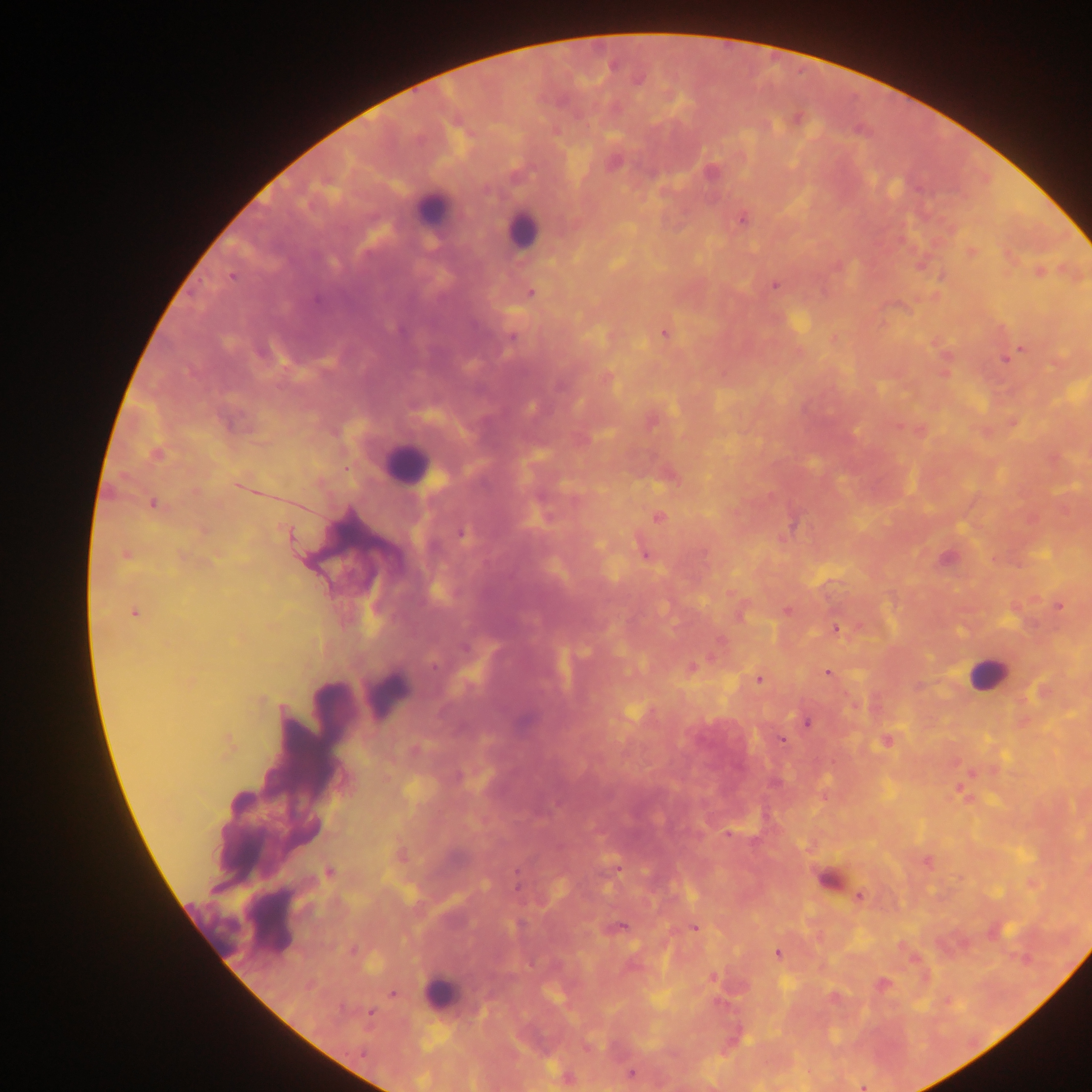
field of view = single
Plasmodium parasite locations = approximate centers as {x, y} in pixels: {612, 66}, {638, 80}, {742, 220}, {972, 253}, {232, 276}, {774, 286}, {530, 293}, {315, 300}, {664, 334}, {511, 338}, {1021, 348}, {1005, 359}, {609, 378}, {156, 454}, {153, 504}, {658, 517}, {462, 532}, {289, 534}, {645, 554}, {126, 556}, {1060, 607}, {787, 611}, {133, 613}, {837, 629}, {720, 640}, {465, 648}, {692, 667}, {827, 673}, {759, 680}, {806, 723}, {782, 741}, {886, 741}, {727, 834}, {329, 872}, {516, 874}, {860, 896}, {622, 927}, {695, 928}, {778, 953}, {883, 984}, {392, 994}, {370, 1013}, {630, 1073}, {863, 1087}
image size = 1092×1092 pixels
preparation = thick blood smear
country = Ghana
capture = mobile-phone photograph through a microscope
leukocyte locations = approximate centers as {x, y} in pixels: {430, 207}, {522, 229}, {406, 465}, {985, 673}, {387, 693}, {440, 993}